Report the malaria status of this cell.
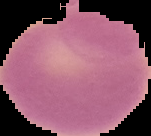
Uninfected.

Summary:
  - Image type: cell region segmented out of the field of view; surrounding area masked to black
  - Preparation: thin blood smear
  - Image size: 151×136 pixels